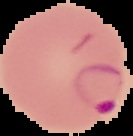

Summary:
  - Image size: 133×136 pixels
  - Image type: cell region segmented out of the field of view; surrounding area masked to black
  - Malaria status: parasitized
  - Preparation: thin blood smear